Classify this cell by malaria status.
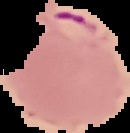

Parasitized.

Summary:
  - Image type: segmented cell region with the area outside set to black
  - Image size: 130×133 pixels
  - Preparation: thin blood film